Assess for malaria.
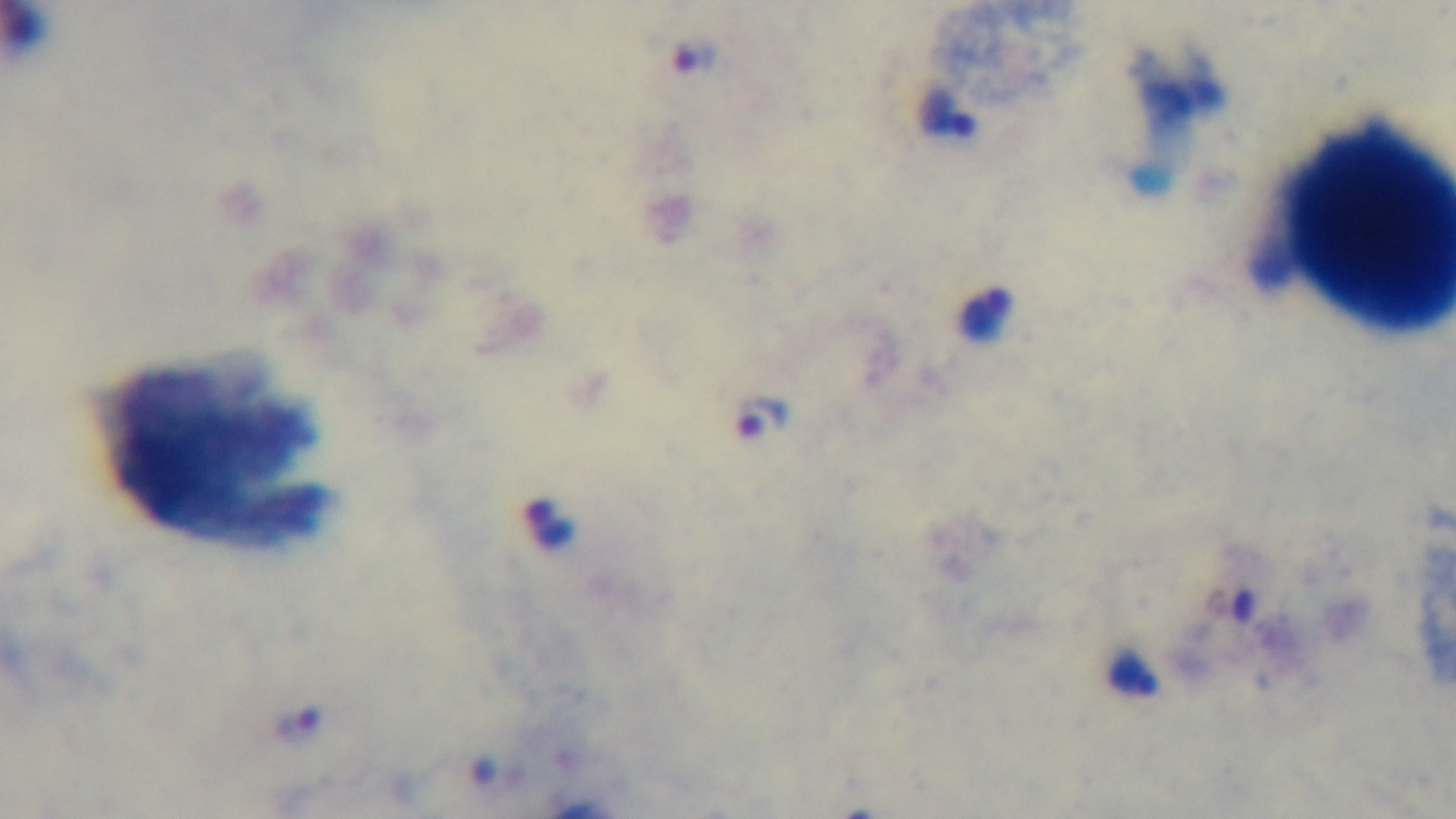

It is infected.

{
  "field_of_view": "one from the slide",
  "stain": "Giemsa",
  "modality": "light microscopy",
  "capture": "mounted 4K digital camera",
  "preparation": "thick blood film",
  "objective": "100x oil immersion"
}